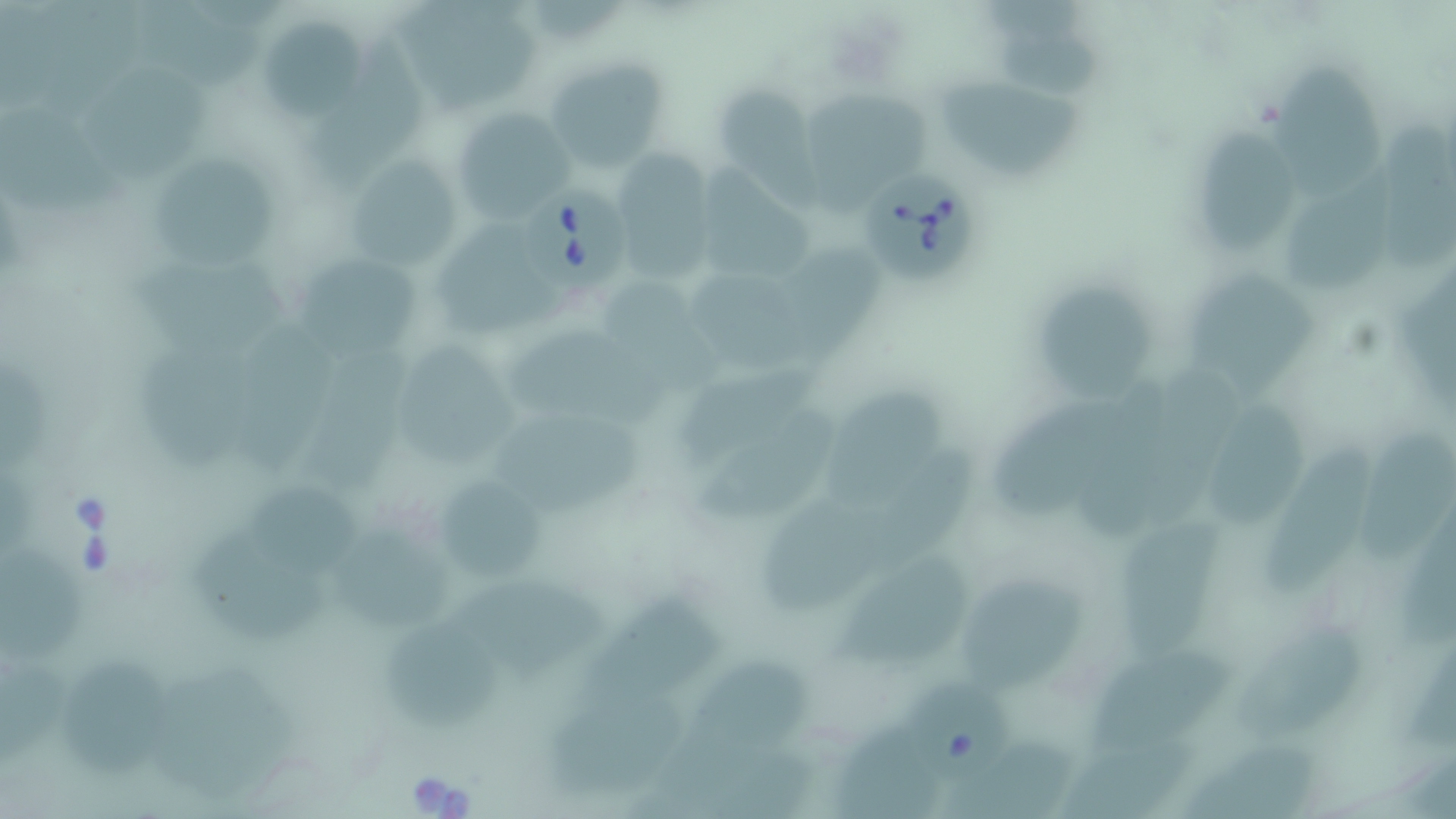

slide_level_diagnosis: Babesia divergens
modality: optical microscopy
field_of_view: one of a larger specimen
image_size: 1456×819 pixels
babesia_divergens_infected_red_blood_cell_locations: 'approximate bounding boxes as named x1/y1/x2/y2 corners in pixels: (x1=859, y1=173, x2=978, y2=286), (x1=528, y1=187, x2=632, y2=291), (x1=916, y1=682, x2=1008, y2=781)'
magnification: 1000x
stain: May-Grünwald-Giemsa
uninfected_red_blood_cell_locations: 'approximate bounding boxes as named x1/y1/x2/y2 corners in pixels: (x1=393, y1=1, x2=543, y2=117), (x1=130, y1=4, x2=269, y2=89), (x1=259, y1=15, x2=367, y2=122), (x1=998, y1=17, x2=1105, y2=98), (x1=310, y1=32, x2=437, y2=192), (x1=544, y1=57, x2=669, y2=172), (x1=1275, y1=65, x2=1385, y2=206), (x1=86, y1=67, x2=214, y2=185), (x1=941, y1=78, x2=1089, y2=184), (x1=712, y1=80, x2=813, y2=183), (x1=799, y1=94, x2=927, y2=209), (x1=0, y1=107, x2=128, y2=212), (x1=451, y1=108, x2=575, y2=223), (x1=1196, y1=126, x2=1301, y2=254), (x1=608, y1=148, x2=718, y2=282), (x1=146, y1=156, x2=289, y2=267), (x1=1282, y1=156, x2=1394, y2=295), (x1=351, y1=157, x2=469, y2=272), (x1=701, y1=162, x2=815, y2=279), (x1=435, y1=219, x2=572, y2=335), (x1=784, y1=245, x2=888, y2=373), (x1=131, y1=253, x2=299, y2=363), (x1=298, y1=258, x2=424, y2=353), (x1=688, y1=264, x2=824, y2=378), (x1=1191, y1=268, x2=1314, y2=397), (x1=1038, y1=281, x2=1154, y2=400), (x1=607, y1=283, x2=728, y2=390), (x1=505, y1=325, x2=669, y2=422), (x1=224, y1=330, x2=336, y2=478), (x1=302, y1=343, x2=426, y2=498), (x1=132, y1=344, x2=256, y2=481), (x1=395, y1=348, x2=520, y2=466), (x1=680, y1=350, x2=837, y2=467), (x1=828, y1=388, x2=952, y2=509), (x1=993, y1=391, x2=1133, y2=525), (x1=702, y1=397, x2=840, y2=523), (x1=1201, y1=398, x2=1306, y2=525), (x1=496, y1=414, x2=646, y2=513), (x1=1363, y1=424, x2=1456, y2=565), (x1=858, y1=441, x2=980, y2=574), (x1=1264, y1=445, x2=1373, y2=597), (x1=434, y1=471, x2=551, y2=590), (x1=759, y1=475, x2=905, y2=622), (x1=244, y1=479, x2=371, y2=578), (x1=1125, y1=513, x2=1219, y2=652), (x1=327, y1=519, x2=464, y2=634), (x1=195, y1=526, x2=330, y2=644), (x1=1, y1=538, x2=89, y2=669), (x1=837, y1=553, x2=976, y2=667), (x1=450, y1=577, x2=604, y2=677), (x1=959, y1=577, x2=1084, y2=697), (x1=585, y1=598, x2=721, y2=721), (x1=384, y1=621, x2=501, y2=731), (x1=1233, y1=630, x2=1362, y2=739), (x1=1085, y1=646, x2=1243, y2=759), (x1=60, y1=656, x2=173, y2=776), (x1=695, y1=658, x2=815, y2=754), (x1=553, y1=687, x2=693, y2=790), (x1=834, y1=724, x2=944, y2=817), (x1=1187, y1=737, x2=1319, y2=819), (x1=943, y1=739, x2=1072, y2=819)'
preparation: thin blood film